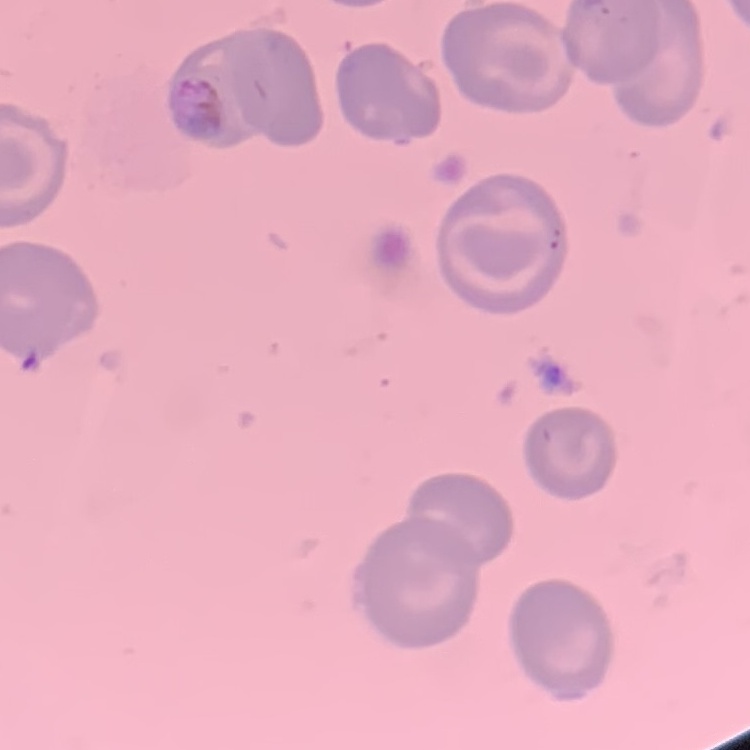 The erythrocytes show no rouleaux formation. Thin peripheral smear. Square crop of a larger photomicrograph. Stained with either Field's or Giemsa.